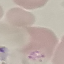
Malaria status: parasitized. Giemsa-stained preparation. Thin blood film. Cell patch, automatically extracted from a larger field of view and resized to 64 × 64 pixels. Photographed with a smartphone camera at the microscope eyepiece.